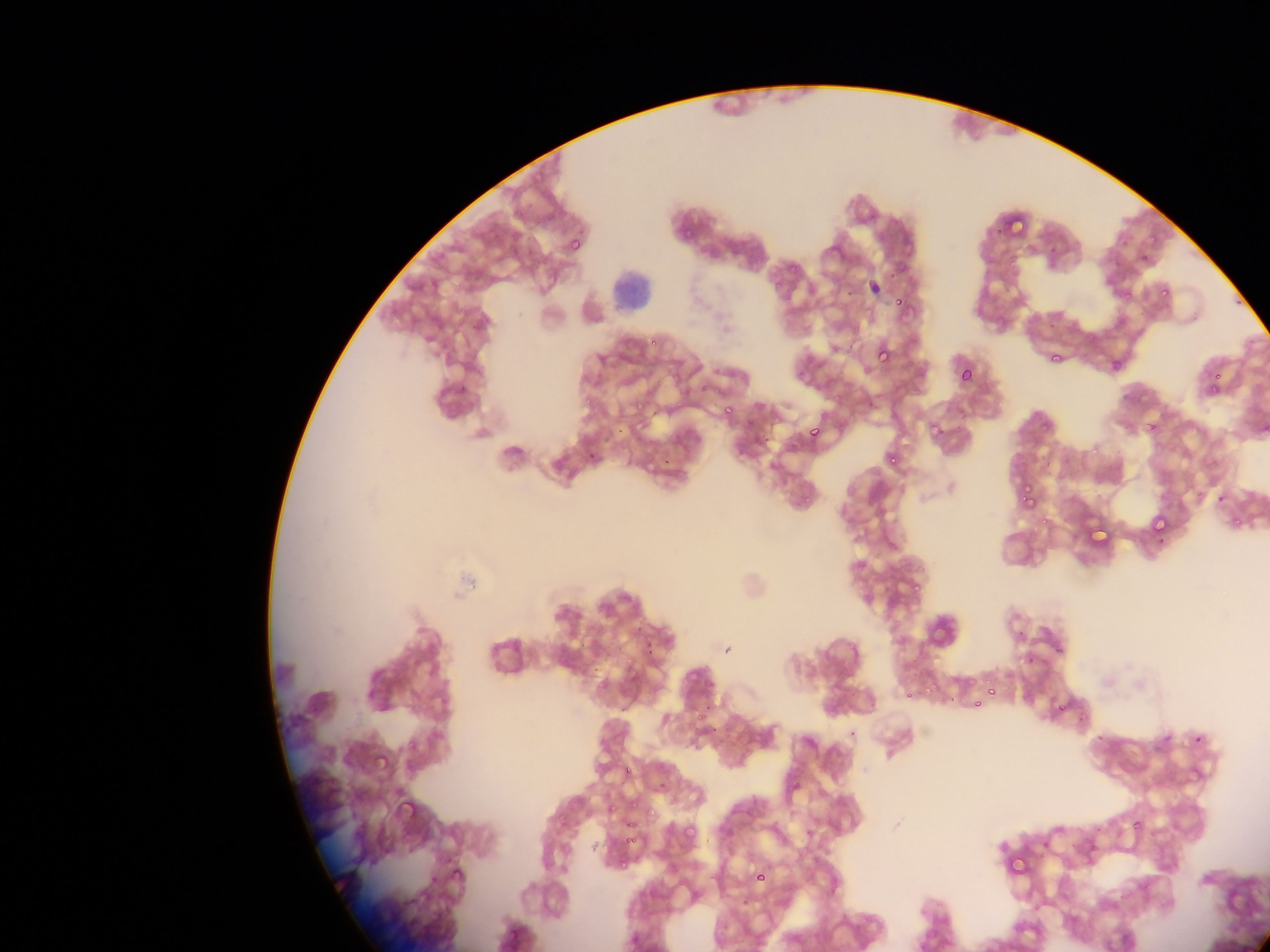
Approximate bounding boxes as (left, top, right, bottom) in pixels.
Summary:
  - Malaria parasite locations: (1007, 210, 1028, 241), (681, 226, 695, 238), (568, 236, 583, 253), (1139, 253, 1150, 265), (790, 259, 804, 273), (1159, 285, 1171, 297), (1122, 290, 1133, 300), (893, 295, 903, 306), (651, 339, 660, 345), (875, 345, 892, 363), (1048, 351, 1062, 364), (790, 357, 816, 387), (959, 366, 975, 383), (668, 370, 679, 385), (1211, 370, 1221, 382), (1207, 372, 1220, 389), (698, 379, 712, 396), (1207, 380, 1222, 394), (582, 394, 594, 406), (723, 406, 733, 417), (744, 417, 755, 428), (1146, 419, 1160, 434), (808, 424, 822, 438), (1091, 440, 1105, 454), (886, 452, 900, 465), (1018, 480, 1038, 505), (1192, 489, 1207, 499), (801, 492, 811, 507), (1021, 496, 1038, 514), (1038, 513, 1051, 530), (1152, 515, 1170, 534), (1231, 517, 1247, 532), (1087, 524, 1114, 545), (909, 580, 924, 593), (644, 631, 660, 654), (1053, 645, 1064, 655), (620, 655, 643, 674), (1026, 655, 1037, 665), (595, 672, 611, 691), (924, 678, 941, 695), (985, 679, 999, 700), (937, 689, 951, 703), (905, 692, 916, 701), (972, 699, 982, 708), (692, 702, 712, 720), (1056, 703, 1067, 714), (1076, 711, 1089, 726), (1094, 731, 1104, 741), (404, 733, 418, 754), (1193, 734, 1203, 743), (370, 749, 398, 774), (623, 766, 633, 777), (392, 791, 421, 824), (624, 795, 637, 809), (644, 800, 663, 817), (606, 804, 617, 814), (621, 810, 639, 827), (557, 815, 569, 828), (623, 818, 635, 829), (1132, 820, 1143, 829), (683, 825, 696, 839), (624, 829, 641, 845), (1009, 852, 1032, 879), (621, 853, 632, 868), (704, 861, 726, 883), (753, 868, 766, 883), (449, 869, 466, 887), (505, 925, 520, 940)
  - Leukocyte locations: (605, 256, 665, 320)
  - Field of view: single
  - Country: Ghana
  - Preparation: thin blood smear
  - Capture: mobile-phone photograph through a microscope
  - Image size: 1270×952 pixels